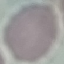

Summary:
  - Result: no malaria parasites seen
  - Image type: cell patch, automatically extracted from a larger field of view and resized to 64 × 64 pixels
  - Stain: Giemsa
  - Preparation: thin blood film
  - Capture: smartphone camera at the microscope eyepiece